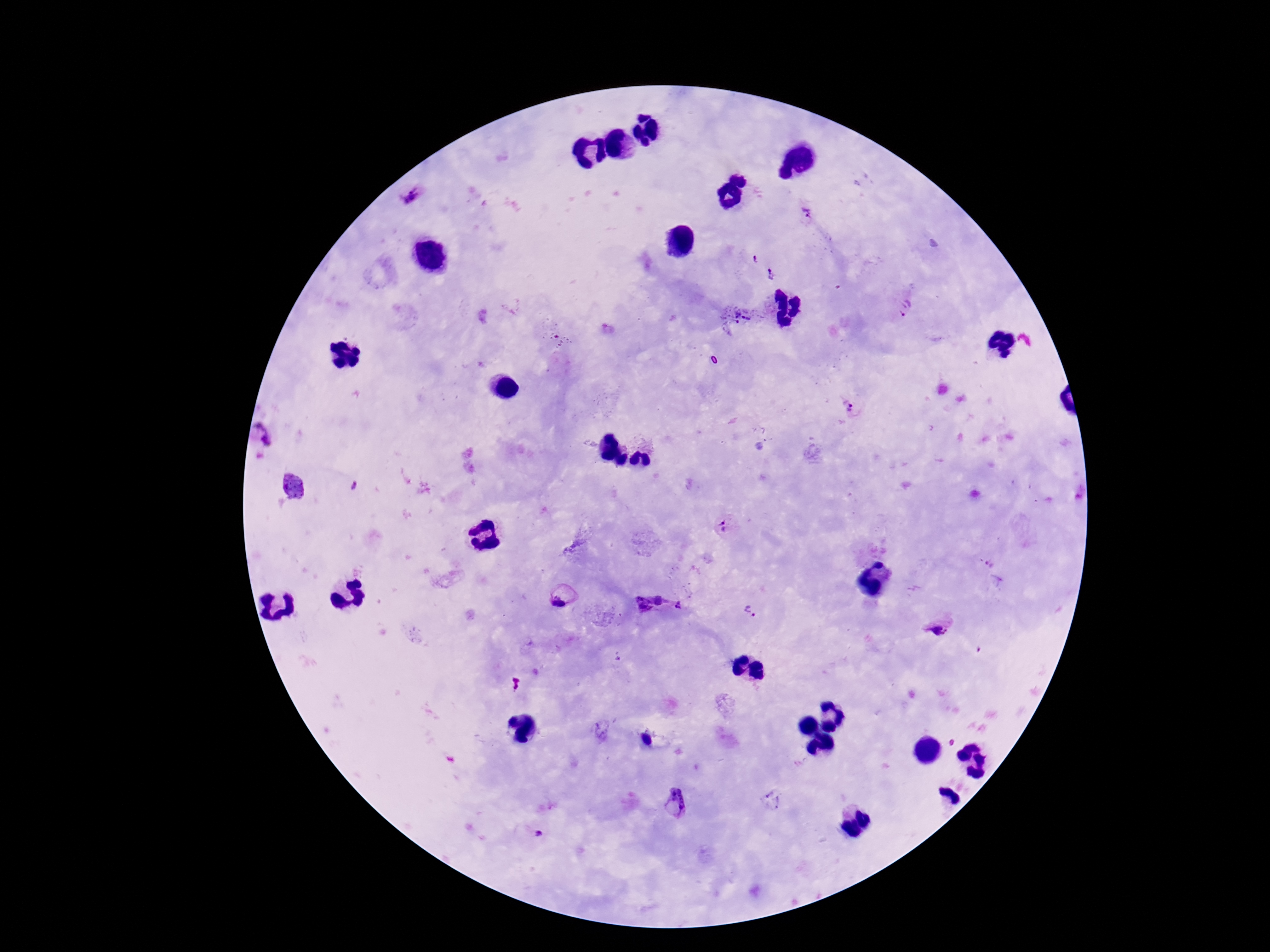

Approximate centers as (x, y) in pixels.
Summary:
  - Plasmodium parasite locations: (410, 198), (806, 214), (755, 258), (771, 275), (905, 309), (739, 314), (557, 340), (848, 407), (265, 435), (292, 487), (354, 487), (725, 526), (990, 563), (559, 598), (648, 602), (678, 605), (752, 612), (939, 627), (600, 732), (773, 799), (675, 803), (539, 832)
  - Capture: smartphone camera through the microscope eyepiece
  - Preparation: thick blood smear
  - Image size: 1270×952 pixels
  - Magnification: 100x
  - Field of view: one from this slide
  - Stain: Giemsa
  - Patient malaria status: positive